Assess the morphology of the erythrocytes.
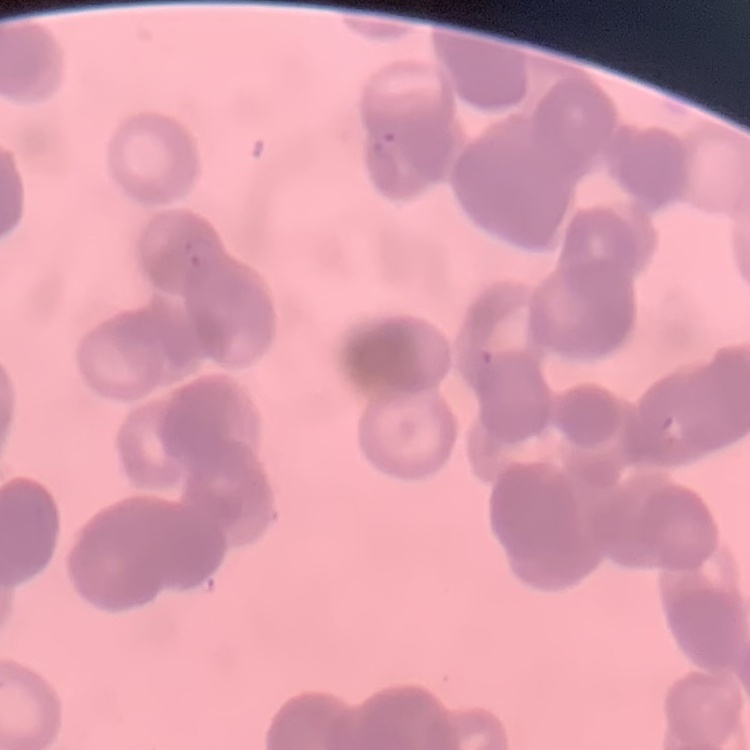
Rouleaux formation.

stain = Field's or Giemsa
image type = square crop of a larger photomicrograph
preparation = thin blood film